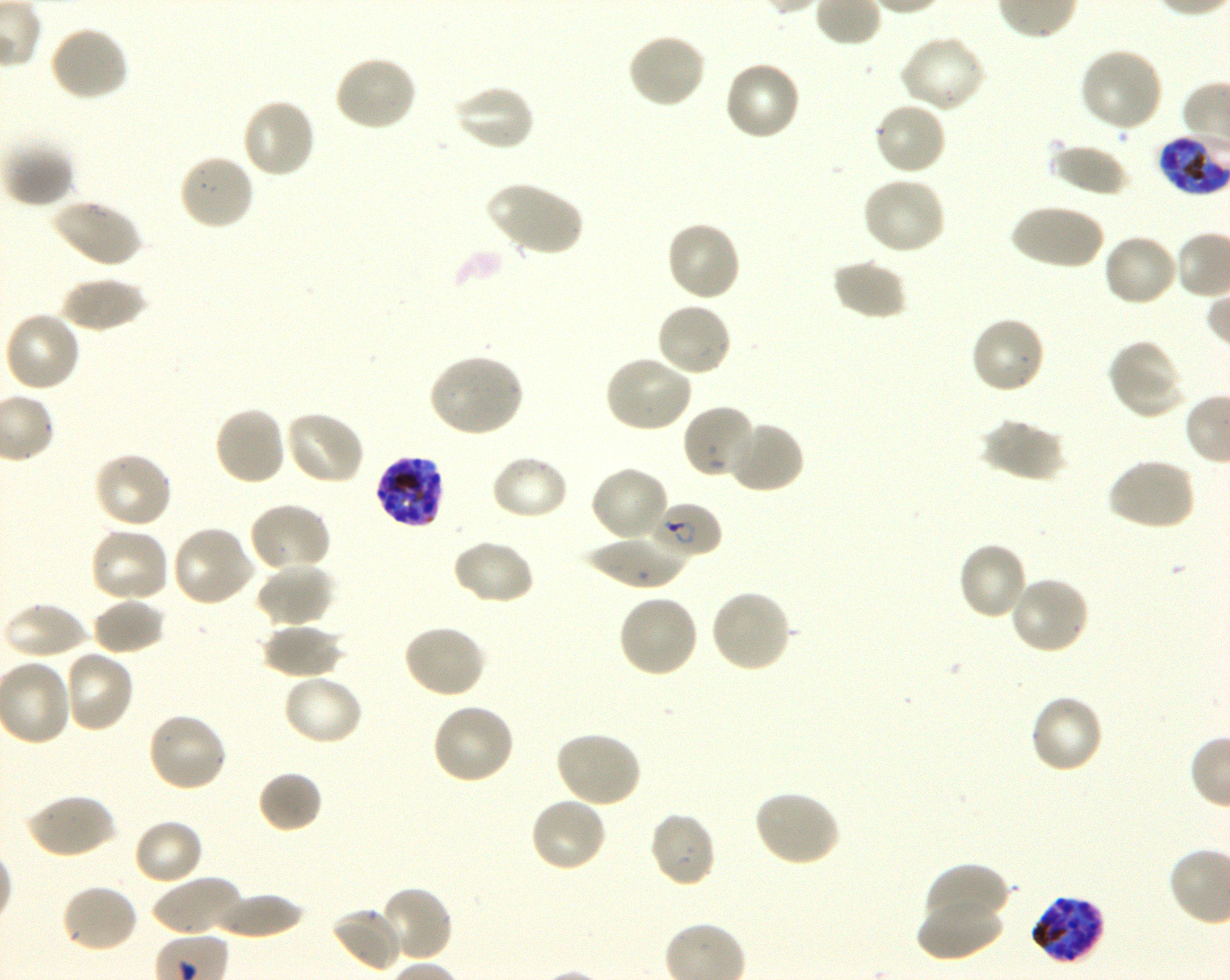
Approximate bounding boxes as {x1, y1, x2, y2} in pixels. Not every red blood cell is marked. A life-cycle stage — or a range of stages, where the recorded stages span more than one — follows each staged infected red blood cell. Locations of infected red blood cells: {1158, 135, 1227, 195} late trophozoite to early schizont; {375, 455, 446, 529} schizont; {655, 503, 723, 558} ring; {1028, 894, 1105, 965} schizont. Locations of uninfected red blood cells: {48, 25, 130, 102}, {627, 32, 707, 110}, {899, 34, 987, 114}, {1078, 47, 1165, 132}, {333, 54, 419, 132}, {722, 60, 801, 142}, {451, 84, 535, 153}, {241, 97, 317, 180}, {873, 101, 948, 177}, {2, 139, 76, 208}, {1050, 142, 1129, 198}, {177, 152, 256, 231}, {861, 175, 948, 256}, {485, 180, 583, 257}, {51, 198, 142, 268}, {1010, 203, 1104, 271}, {665, 220, 742, 302}, {1102, 232, 1179, 308}, {831, 258, 907, 321}, {59, 276, 147, 332}, {655, 301, 733, 378}, {3, 310, 83, 393}, {970, 316, 1046, 396}, {1108, 340, 1186, 419}, {428, 354, 525, 437}, {603, 355, 694, 434}, {681, 404, 757, 481}, {213, 405, 288, 487}, {283, 409, 367, 486}, {980, 417, 1066, 482}, {726, 420, 806, 494}, {92, 451, 173, 530}, {489, 453, 570, 521}, {1106, 457, 1196, 532}, {590, 465, 670, 544}, {248, 502, 332, 574}, {171, 524, 257, 608}, {88, 525, 172, 604}, {582, 534, 692, 589}, {452, 538, 535, 607}, {956, 542, 1029, 622}, {256, 563, 336, 628}, {1008, 575, 1091, 656}, {709, 588, 792, 673}, {617, 593, 700, 678}, {92, 597, 166, 655}, {3, 600, 88, 661}, {261, 622, 344, 679}, {402, 623, 487, 699}, {62, 648, 136, 733}, {282, 673, 364, 747}, {1028, 693, 1104, 774}, {431, 702, 516, 786}, {147, 710, 229, 793}, {554, 729, 643, 808}, {257, 769, 323, 834}, {754, 789, 842, 866}, {26, 793, 117, 860}, {528, 796, 608, 873}, {648, 810, 717, 888}, {133, 819, 205, 886}, {922, 862, 1010, 931}, {152, 874, 243, 938}, {60, 882, 140, 954}, {379, 885, 455, 963}, {211, 891, 305, 938}, {917, 895, 1005, 962}, {330, 906, 405, 973}. Life-cycle stages observed: ring, schizont. Plasmodium falciparum strain 3D7 maintained in shaking in-vitro culture. Oil immersion, 100x objective (numerical aperture 1.30). Single field of view. Thin blood smear. Giemsa-stained preparation. Donor blood group O+. Image is 1230×980 pixels.